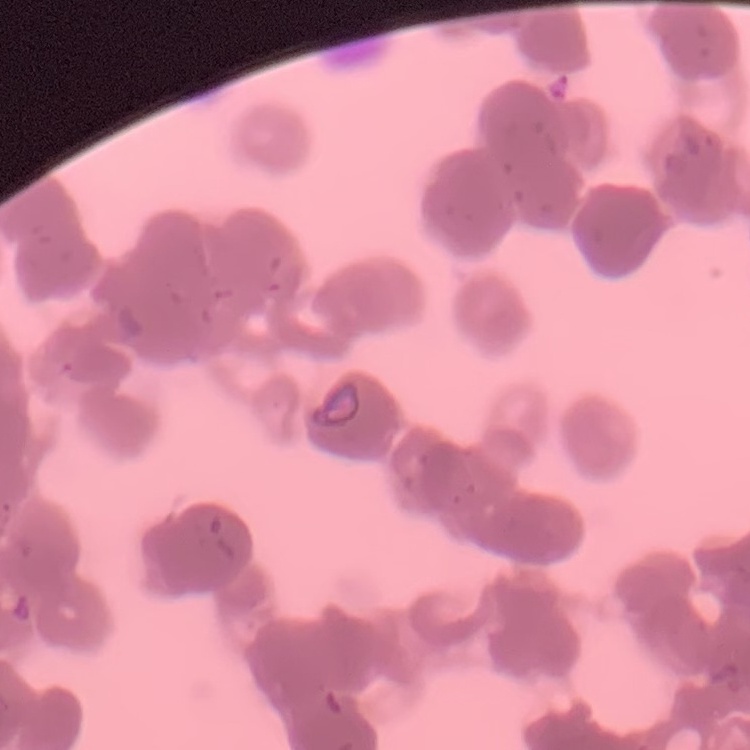 The erythrocytes exhibit rouleaux formation. Stained with either Field's or Giemsa. One tile cut from a larger photomicrograph. Thin blood smear.